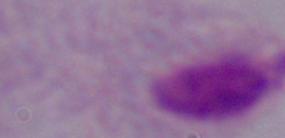 1000x magnification. Micrograph. A trichomonad is seen.